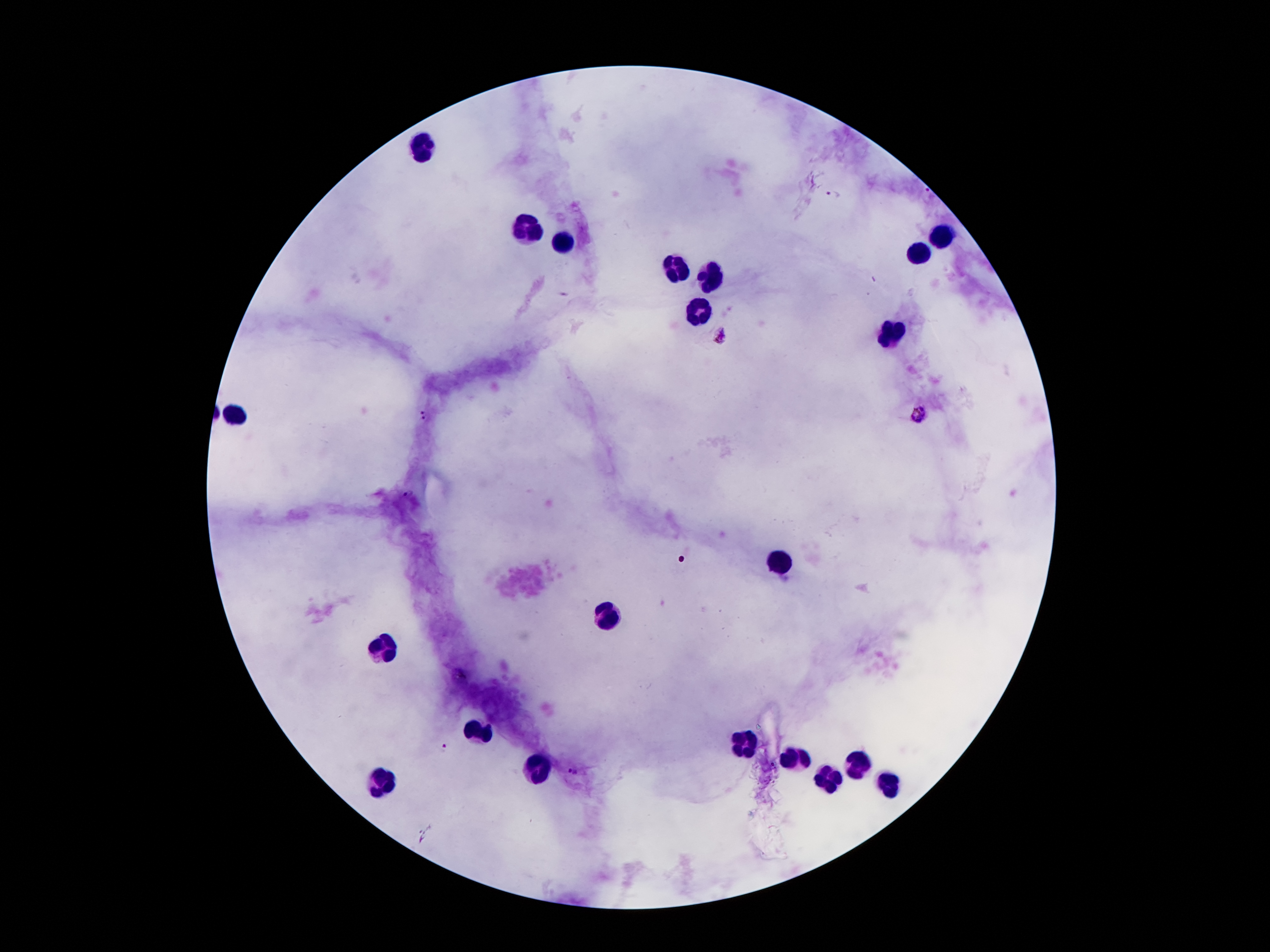
coordinate format = approximate centers as {x, y} in pixels
malaria parasite locations = {834, 194}, {722, 336}, {919, 412}, {425, 413}, {445, 747}, {572, 772}
leukocyte locations = {422, 144}, {531, 231}, {947, 236}, {567, 245}, {915, 256}, {681, 272}, {710, 276}, {699, 311}, {894, 336}, {231, 417}, {785, 562}, {611, 613}, {381, 651}, {477, 731}, {744, 749}, {797, 763}, {540, 765}, {858, 765}, {383, 781}, {829, 783}, {890, 783}
magnification = 100x
field of view = single
capture = smartphone through the microscope eyepiece
preparation = thick peripheral-blood smear
stain = Giemsa
image size = 1270×952 pixels
patient malaria status = positive for Plasmodium falciparum